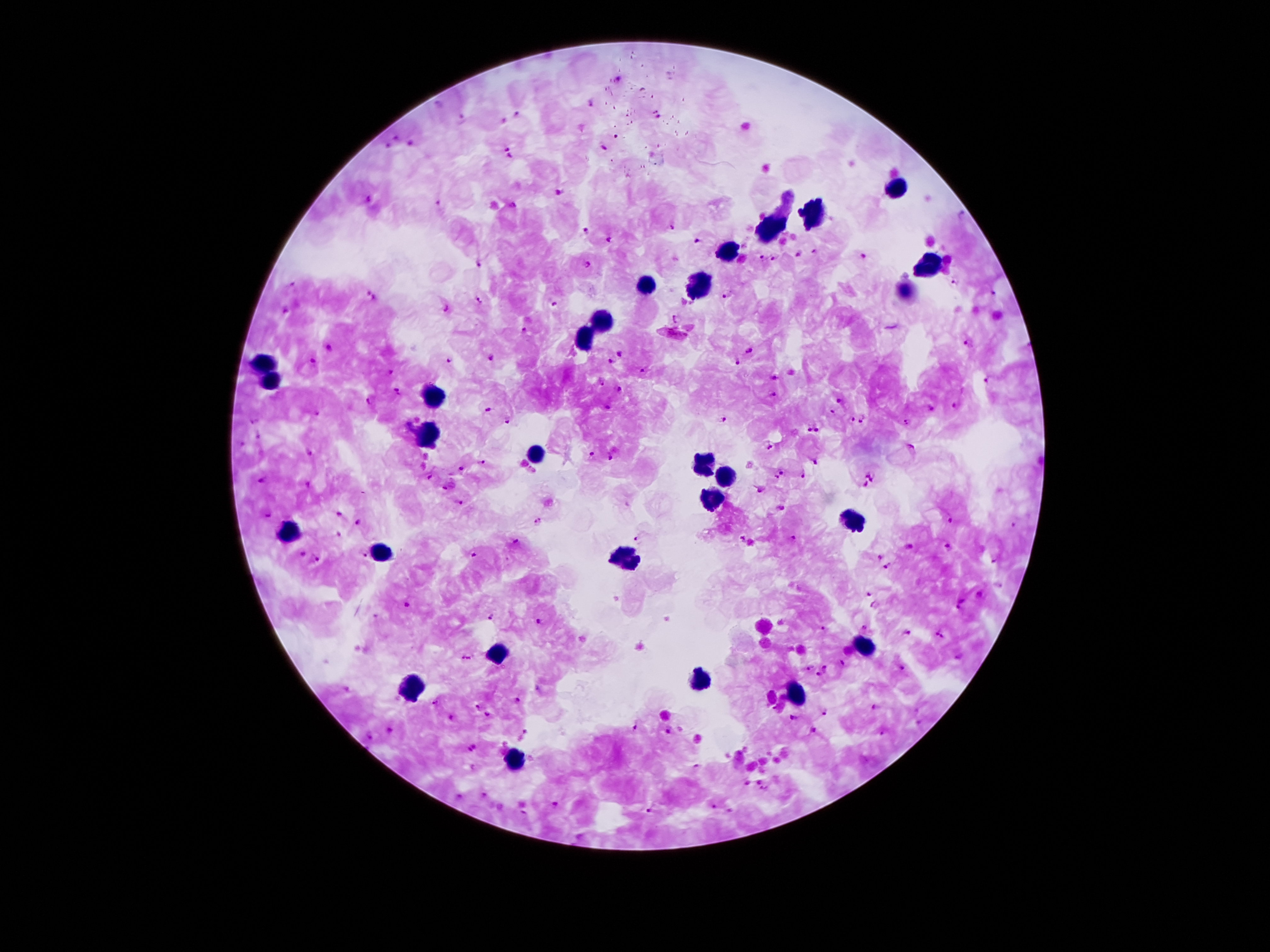
{
  "capture": "smartphone through the microscope eyepiece",
  "preparation": "thick blood smear",
  "malaria_parasite_locations": "approximate centers as [x, y] in pixels: [618, 78], [589, 104], [439, 105], [658, 115], [516, 116], [461, 119], [504, 121], [398, 137], [616, 137], [389, 145], [410, 145], [604, 148], [508, 152], [557, 192], [369, 200], [440, 204], [960, 215], [669, 227], [587, 230], [610, 240], [698, 242], [813, 251], [798, 253], [863, 257], [760, 259], [774, 260], [479, 265], [588, 266], [955, 282], [293, 285], [727, 295], [993, 296], [370, 297], [477, 299], [554, 303], [445, 309], [287, 310], [678, 319], [524, 332], [678, 333], [969, 344], [328, 349], [750, 351], [619, 354], [491, 357], [447, 360], [611, 361], [737, 361], [313, 363], [641, 371], [388, 374], [774, 377], [989, 380], [600, 381], [620, 390], [398, 392], [773, 395], [840, 401], [369, 402], [608, 407], [952, 408], [488, 409], [930, 409], [833, 412], [315, 413], [508, 418], [853, 418], [863, 419], [254, 420], [724, 420], [907, 423], [807, 428], [819, 429], [259, 435], [241, 444], [769, 445], [911, 448], [309, 454], [592, 455], [611, 459], [814, 459], [480, 463], [461, 470], [866, 472], [782, 473], [803, 476], [430, 477], [777, 477], [874, 480], [263, 481], [309, 485], [864, 487], [442, 488], [760, 488], [461, 503], [337, 513], [266, 515], [949, 521], [359, 522], [537, 523], [1013, 524], [339, 535], [741, 538], [791, 538], [514, 541], [637, 541], [909, 547], [949, 547], [364, 554], [303, 555], [472, 556], [880, 558], [316, 559], [887, 567], [868, 595], [978, 595], [405, 604], [876, 605], [962, 605], [491, 616], [539, 622], [863, 627], [825, 629], [907, 632], [940, 635], [957, 658], [465, 659], [842, 663], [808, 668], [827, 668], [902, 668], [817, 676], [540, 689], [516, 700], [438, 702], [476, 706], [873, 707], [824, 712], [487, 715], [452, 718], [793, 718], [636, 727], [668, 730], [813, 730], [391, 732], [525, 734], [882, 734], [369, 737], [472, 748], [697, 766], [764, 788], [484, 795], [460, 797], [556, 807], [714, 807], [649, 811]",
  "stain": "Giemsa",
  "leukocyte_locations": "approximate centers as [x, y] in pixels: [894, 185], [812, 212], [767, 232], [726, 255], [922, 265], [700, 285], [646, 286], [906, 290], [601, 321], [588, 339], [267, 367], [272, 384], [436, 400], [428, 437], [535, 455], [703, 465], [726, 479], [710, 499], [853, 521], [288, 530], [380, 553], [623, 556], [865, 647], [496, 656], [700, 683], [415, 688], [797, 695], [512, 762]",
  "image_size": "1270×952 pixels",
  "magnification": "100x",
  "field_of_view": "single",
  "patient_malaria_status": "positive for Plasmodium falciparum"
}